State which cell type is depicted.
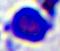

A leukocyte.

Summary:
  - Magnification: 400x
  - Modality: photomicrograph